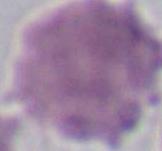 An erythrocyte is shown. Micrograph. 1000x magnification.